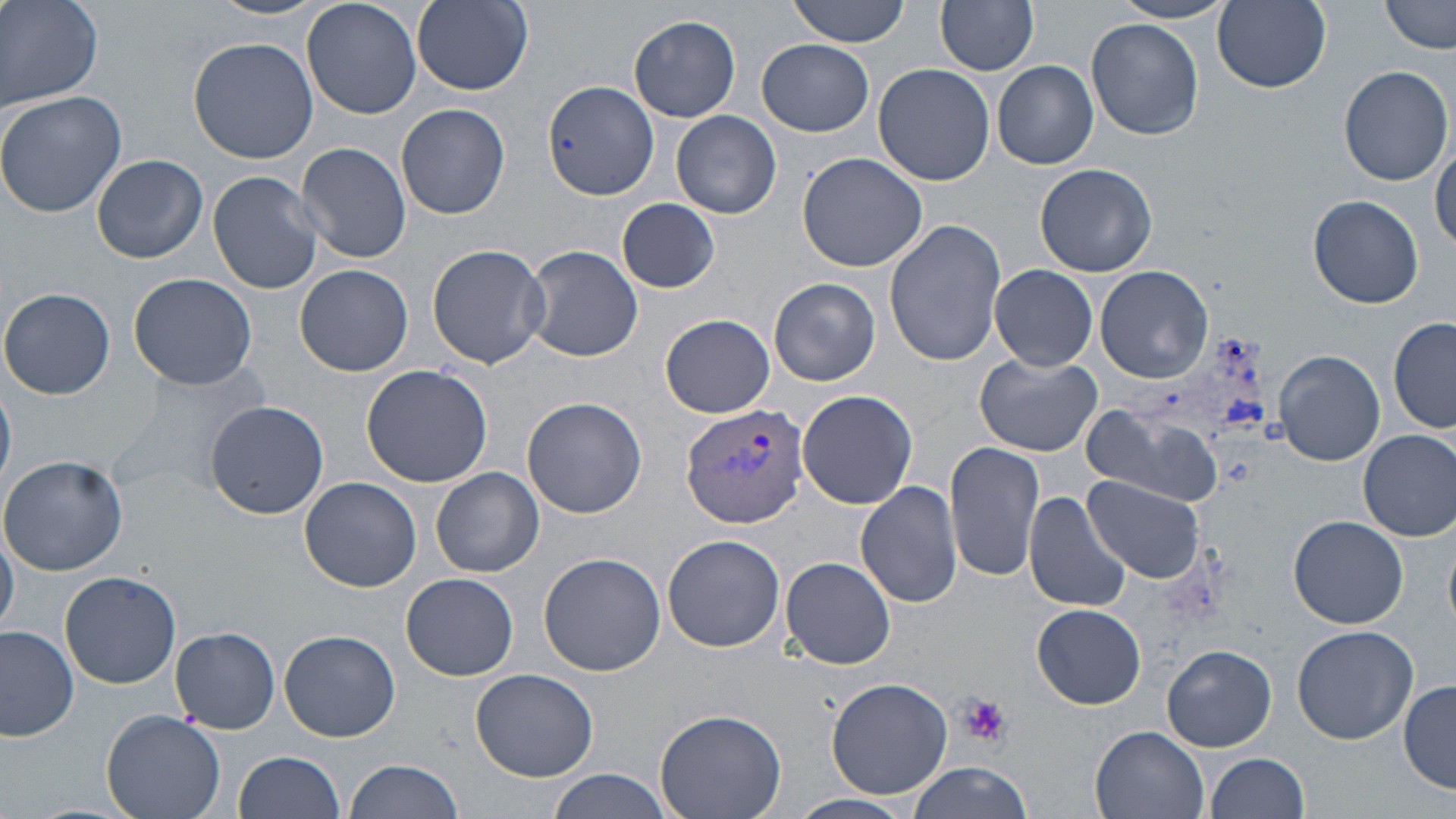
slide_level_diagnosis: Plasmodium vivax
platelet_locations: 'approximate bounding boxes as [x1, y1, x2, y2] in pixels: [957, 694, 1013, 747]'
stain: May-Grünwald-Giemsa
modality: light microscopy
field_of_view: one of a larger specimen
magnification: 1000x
preparation: thin blood smear
image_size: 1456×819 pixels
uninfected_red_blood_cell_locations: 'approximate bounding boxes as [x1, y1, x2, y2] in pixels: [0, 0, 104, 112], [209, 0, 326, 20], [303, 0, 423, 119], [410, 0, 535, 99], [789, 0, 911, 46], [937, 0, 1039, 74], [1210, 0, 1333, 95], [1382, 0, 1456, 54], [1109, 1, 1235, 24], [627, 15, 741, 120], [1086, 19, 1204, 139], [188, 37, 320, 164], [758, 40, 874, 135], [992, 62, 1098, 169], [874, 64, 995, 186], [1339, 65, 1452, 185], [543, 80, 658, 202], [0, 90, 129, 218], [395, 103, 512, 219], [670, 110, 782, 219], [1433, 137, 1456, 254], [296, 141, 410, 263], [798, 153, 931, 274], [92, 154, 208, 263], [1034, 163, 1157, 277], [207, 170, 324, 294], [1308, 194, 1425, 309], [616, 198, 720, 294], [883, 218, 1006, 369], [427, 244, 550, 369], [521, 244, 644, 362], [296, 265, 415, 377], [990, 265, 1098, 370], [1095, 266, 1211, 383], [127, 272, 257, 390], [769, 278, 881, 386], [0, 286, 118, 399], [661, 314, 775, 417], [1390, 317, 1456, 435], [1274, 351, 1385, 466], [976, 353, 1102, 457], [360, 362, 496, 487], [110, 366, 265, 499], [0, 378, 16, 493], [798, 389, 918, 509], [522, 396, 649, 519], [205, 400, 329, 519], [1082, 403, 1225, 507], [1358, 428, 1456, 541], [945, 441, 1045, 582], [0, 452, 129, 575], [430, 467, 544, 578], [1084, 475, 1206, 584], [299, 476, 422, 592], [855, 480, 963, 608], [1023, 491, 1131, 613], [1289, 515, 1409, 629], [0, 522, 19, 638], [663, 533, 785, 652], [539, 552, 668, 677], [782, 558, 895, 670], [59, 570, 181, 688], [402, 574, 519, 680], [1032, 604, 1144, 709], [0, 625, 79, 742], [170, 625, 280, 734], [1291, 626, 1418, 747], [280, 631, 401, 741], [1162, 646, 1276, 752], [472, 669, 598, 782], [826, 676, 954, 799], [1399, 680, 1456, 792], [101, 708, 229, 819], [656, 708, 787, 819], [1090, 725, 1210, 819], [232, 750, 346, 819], [1207, 753, 1311, 818], [343, 758, 465, 819], [907, 762, 1038, 818], [547, 771, 676, 819], [786, 794, 921, 819]'
plasmodium_vivax_infected_red_blood_cell_locations: 'approximate bounding boxes as [x1, y1, x2, y2] in pixels: [680, 402, 811, 531]'